Describe the morphology of the red blood cells.
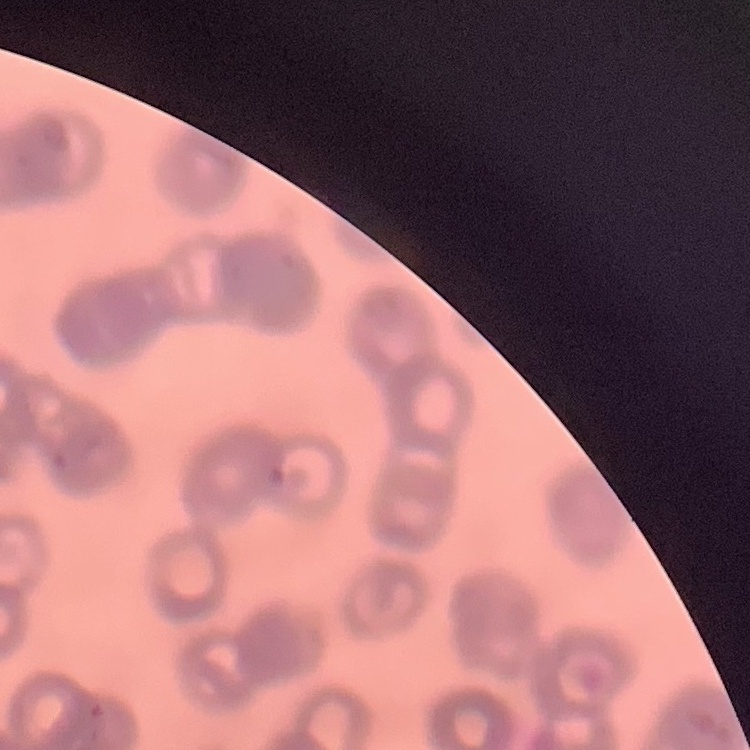

They show rouleaux formation.

Summary:
  - Preparation: thin peripheral smear
  - Stain: Field's or Giemsa
  - Image type: square crop of a larger photomicrograph